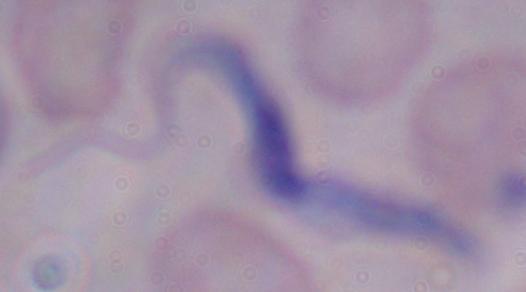

modality = micrograph
magnification = 1000x
identification = trypanosome